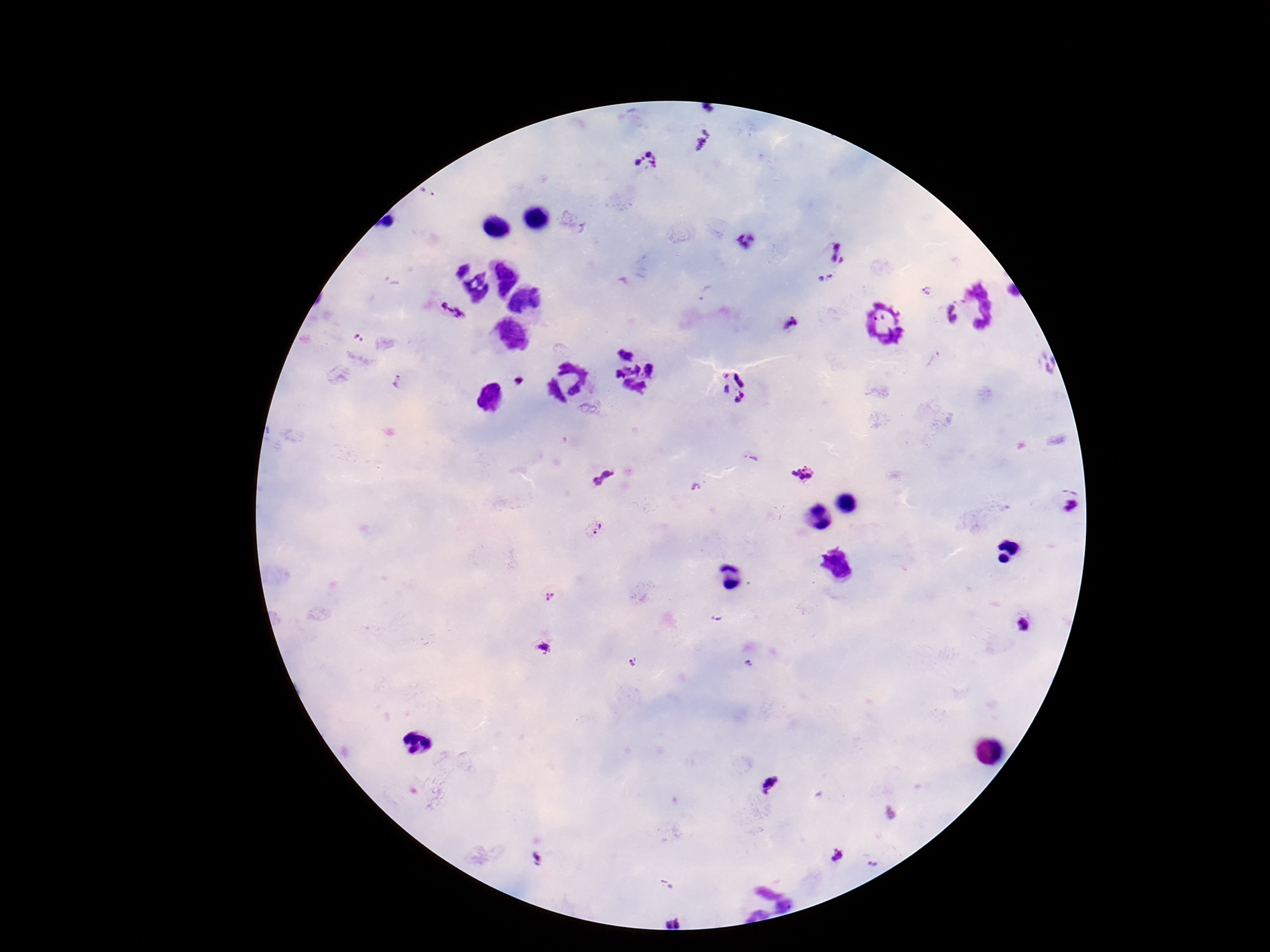

preparation = thick blood smear
stain = Giemsa
patient malaria status = positive
Plasmodium parasite locations = approximate centers as {x, y} in pixels: {704, 139}, {647, 161}, {428, 195}, {840, 251}, {826, 278}, {925, 291}, {450, 310}, {952, 314}, {792, 325}, {358, 340}, {519, 381}, {397, 382}, {731, 385}, {753, 458}, {601, 475}, {804, 476}, {698, 487}, {1068, 508}, {595, 528}, {550, 597}, {717, 619}, {1028, 624}, {542, 648}, {633, 662}, {748, 664}, {772, 784}, {837, 856}, {538, 861}, {873, 864}, {666, 884}
field of view = one from this slide
image size = 1270×952 pixels
magnification = 100x
capture = smartphone camera through the microscope eyepiece